Locate every Plasmodium parasite and every leukocyte.
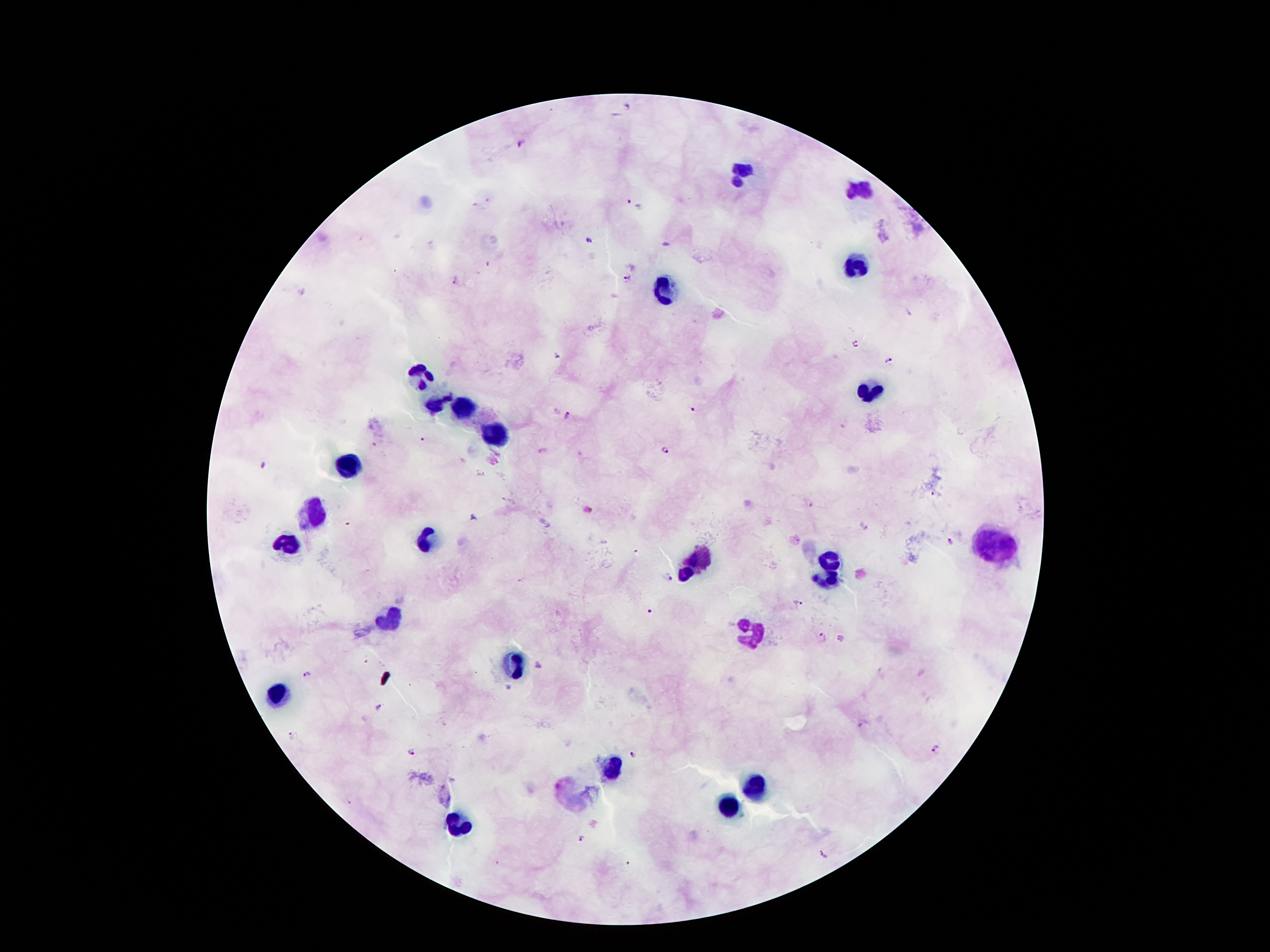
Approximate object centers, in pixels from the top-left corner.
Plasmodium parasites: (x=628, y=106), (x=519, y=144), (x=629, y=202), (x=590, y=241), (x=627, y=277), (x=456, y=280), (x=855, y=344), (x=557, y=356), (x=889, y=360), (x=692, y=410), (x=567, y=414), (x=424, y=440), (x=664, y=450), (x=264, y=466), (x=936, y=494), (x=810, y=504), (x=588, y=512), (x=473, y=517), (x=863, y=526), (x=951, y=542), (x=668, y=577), (x=798, y=603), (x=649, y=611), (x=821, y=637), (x=840, y=638), (x=538, y=665), (x=306, y=674), (x=507, y=686), (x=378, y=707), (x=861, y=724), (x=936, y=748), (x=410, y=751), (x=632, y=754), (x=582, y=839), (x=825, y=854).
Leukocytes: (x=745, y=170), (x=862, y=189), (x=853, y=265), (x=669, y=292), (x=417, y=369), (x=868, y=392), (x=431, y=402), (x=464, y=412), (x=495, y=433), (x=349, y=465), (x=312, y=515), (x=425, y=541), (x=990, y=546), (x=288, y=548), (x=700, y=557), (x=832, y=561), (x=687, y=574), (x=830, y=582), (x=390, y=619), (x=751, y=635), (x=518, y=668), (x=279, y=694), (x=609, y=766), (x=755, y=788), (x=729, y=808), (x=455, y=828).

stain: Giemsa
field_of_view: single
capture: smartphone camera through the microscope eyepiece
image_size: 1270×952 pixels
preparation: thick peripheral-blood smear
patient_malaria_status: infected with Plasmodium falciparum
magnification: 100x